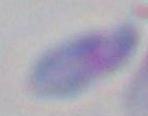
Photomicrograph. Toxoplasma gondii is seen. Captured at 1000x magnification.